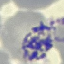

malaria_status: parasitized
preparation: thin smear
capture: smartphone through the microscope eyepiece
stain: Giemsa
image_type: automatically extracted cell patch, resized to 64 × 64 pixels